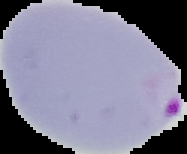

image_type: segmented cell region with the area outside set to black
result: malaria parasites identified
preparation: thin blood film
image_size: 187×154 pixels